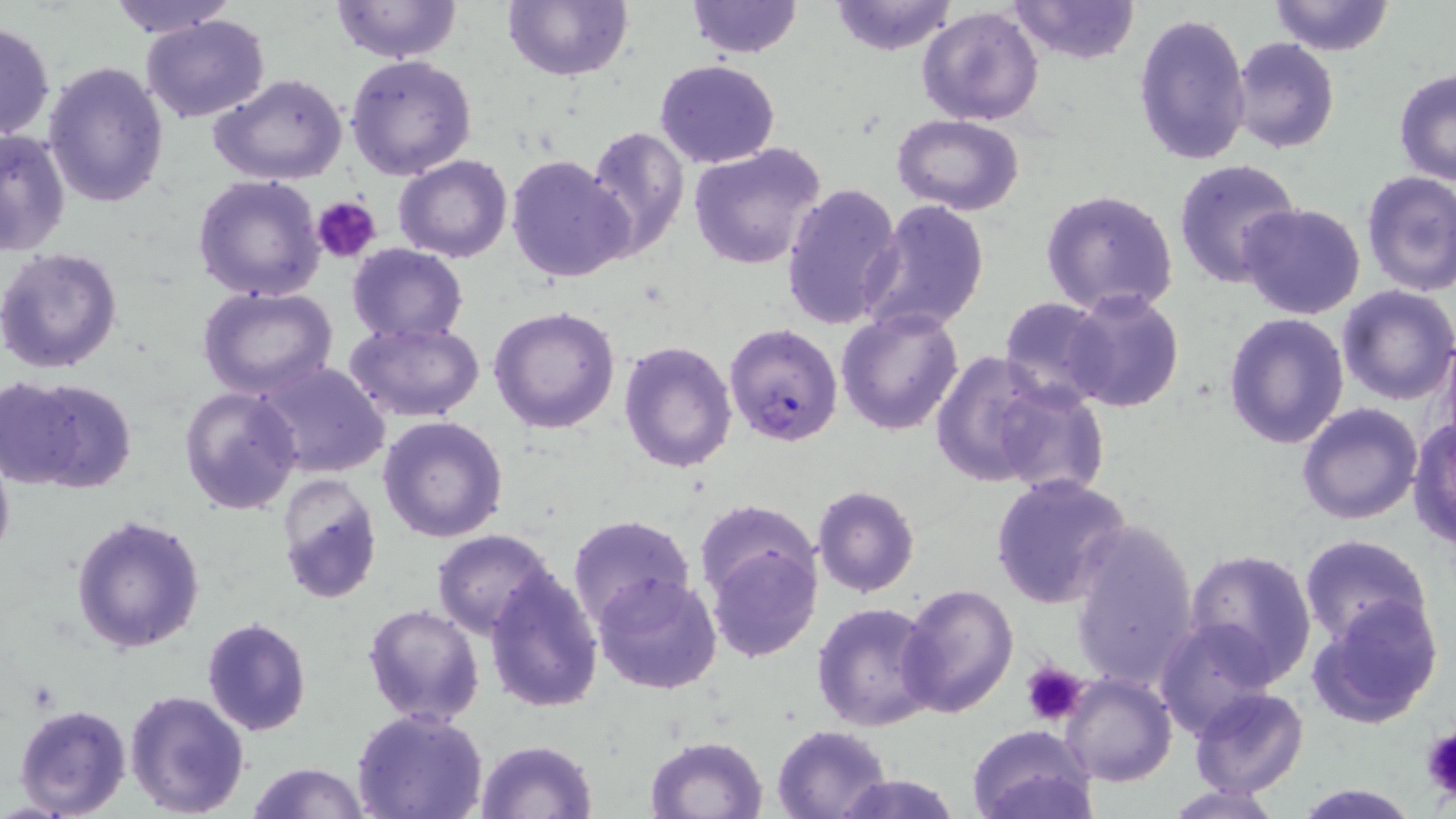

Summary:
  - Coordinate format: approximate bounding boxes as named x1/y1/x2/y2 corners in pixels
  - Platelet locations: (x1=313, y1=197, x2=382, y2=266), (x1=1023, y1=660, x2=1088, y2=727), (x1=1419, y1=728, x2=1455, y2=797)
  - Plasmodium falciparum-infected red blood cell locations: (x1=724, y1=322, x2=845, y2=446)
  - Uninfected red blood cell locations: (x1=102, y1=0, x2=243, y2=39), (x1=331, y1=0, x2=462, y2=64), (x1=684, y1=0, x2=804, y2=57), (x1=1008, y1=0, x2=1140, y2=66), (x1=1265, y1=0, x2=1397, y2=55), (x1=502, y1=1, x2=633, y2=82), (x1=826, y1=1, x2=961, y2=55), (x1=917, y1=6, x2=1044, y2=126), (x1=1133, y1=12, x2=1253, y2=167), (x1=139, y1=14, x2=270, y2=124), (x1=0, y1=19, x2=56, y2=141), (x1=1230, y1=37, x2=1340, y2=153), (x1=345, y1=53, x2=478, y2=180), (x1=655, y1=59, x2=780, y2=168), (x1=42, y1=60, x2=170, y2=209), (x1=1393, y1=67, x2=1456, y2=185), (x1=210, y1=73, x2=350, y2=185), (x1=892, y1=115, x2=1024, y2=216), (x1=583, y1=126, x2=689, y2=258), (x1=0, y1=128, x2=71, y2=257), (x1=688, y1=143, x2=825, y2=270), (x1=393, y1=154, x2=513, y2=263), (x1=505, y1=154, x2=634, y2=284), (x1=1172, y1=157, x2=1304, y2=290), (x1=1360, y1=171, x2=1456, y2=296), (x1=192, y1=175, x2=327, y2=301), (x1=783, y1=182, x2=903, y2=331), (x1=1268, y1=184, x2=1456, y2=307), (x1=1040, y1=189, x2=1181, y2=318), (x1=863, y1=199, x2=990, y2=336), (x1=1237, y1=202, x2=1366, y2=318), (x1=344, y1=243, x2=470, y2=343), (x1=0, y1=246, x2=123, y2=375), (x1=1335, y1=285, x2=1456, y2=405), (x1=198, y1=287, x2=337, y2=400), (x1=1061, y1=290, x2=1185, y2=412), (x1=998, y1=296, x2=1113, y2=409), (x1=489, y1=305, x2=621, y2=433), (x1=835, y1=307, x2=964, y2=435), (x1=1222, y1=313, x2=1349, y2=449), (x1=344, y1=320, x2=485, y2=423), (x1=1439, y1=332, x2=1456, y2=453), (x1=618, y1=341, x2=737, y2=473), (x1=929, y1=351, x2=1055, y2=487), (x1=254, y1=362, x2=391, y2=478), (x1=4, y1=376, x2=138, y2=494), (x1=989, y1=383, x2=1108, y2=497), (x1=178, y1=385, x2=304, y2=514), (x1=1296, y1=402, x2=1423, y2=524), (x1=378, y1=415, x2=508, y2=541), (x1=1408, y1=416, x2=1456, y2=552), (x1=0, y1=447, x2=14, y2=573), (x1=275, y1=473, x2=383, y2=605), (x1=989, y1=474, x2=1130, y2=608), (x1=812, y1=486, x2=921, y2=598), (x1=694, y1=501, x2=821, y2=608), (x1=69, y1=514, x2=207, y2=654), (x1=566, y1=514, x2=695, y2=634), (x1=1068, y1=520, x2=1201, y2=690), (x1=431, y1=530, x2=557, y2=639), (x1=1298, y1=534, x2=1434, y2=647), (x1=707, y1=541, x2=821, y2=663), (x1=1184, y1=548, x2=1317, y2=687), (x1=483, y1=568, x2=604, y2=713), (x1=593, y1=574, x2=724, y2=696), (x1=897, y1=584, x2=1019, y2=718), (x1=1308, y1=598, x2=1444, y2=729), (x1=811, y1=601, x2=939, y2=732), (x1=361, y1=604, x2=485, y2=727), (x1=202, y1=616, x2=313, y2=736), (x1=1153, y1=619, x2=1276, y2=740), (x1=1060, y1=673, x2=1176, y2=786), (x1=1188, y1=687, x2=1308, y2=800), (x1=124, y1=689, x2=251, y2=817), (x1=12, y1=701, x2=132, y2=819), (x1=352, y1=709, x2=490, y2=819), (x1=771, y1=724, x2=892, y2=818), (x1=966, y1=725, x2=1097, y2=819), (x1=645, y1=735, x2=768, y2=818), (x1=477, y1=740, x2=597, y2=818), (x1=244, y1=761, x2=370, y2=819), (x1=835, y1=773, x2=961, y2=818), (x1=1291, y1=781, x2=1425, y2=818), (x1=1163, y1=785, x2=1284, y2=818)
  - Slide-level diagnosis: Plasmodium falciparum
  - Preparation: thin blood smear
  - Modality: light microscopy
  - Stain: May-Grünwald-Giemsa
  - Field of view: one of a larger specimen
  - Image size: 1456×819 pixels
  - Magnification: 1000x